Assess the morphology of the red blood cells.
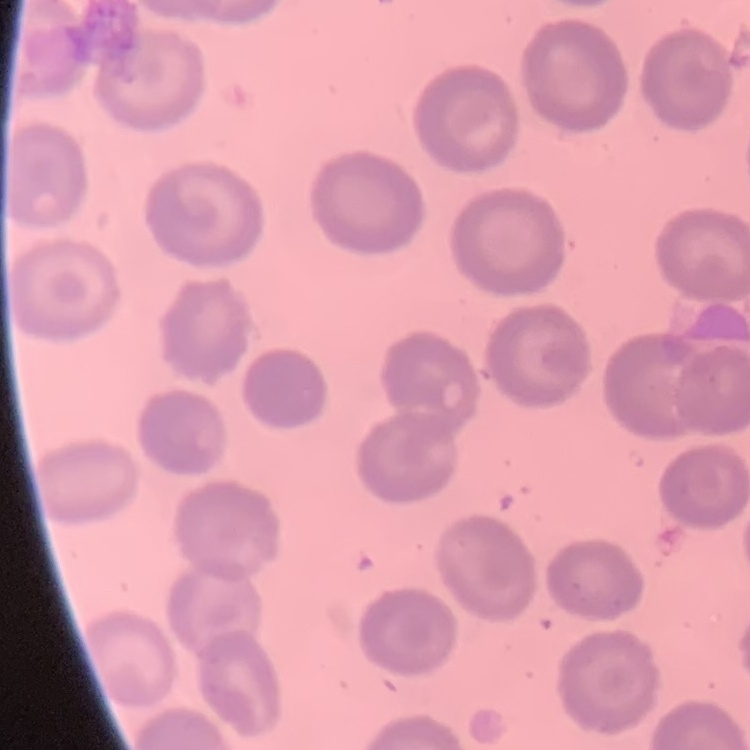
No rouleaux formation.

preparation = thin blood film
image type = square crop of a larger photomicrograph
stain = Field's or Giemsa